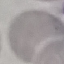

result: no malaria parasites detected
stain: Giemsa
capture: smartphone camera at the microscope eyepiece
image_type: cell patch, automatically extracted from a larger field of view and resized to 64 × 64 pixels
preparation: thin smear